Describe the morphology of the red blood cells.
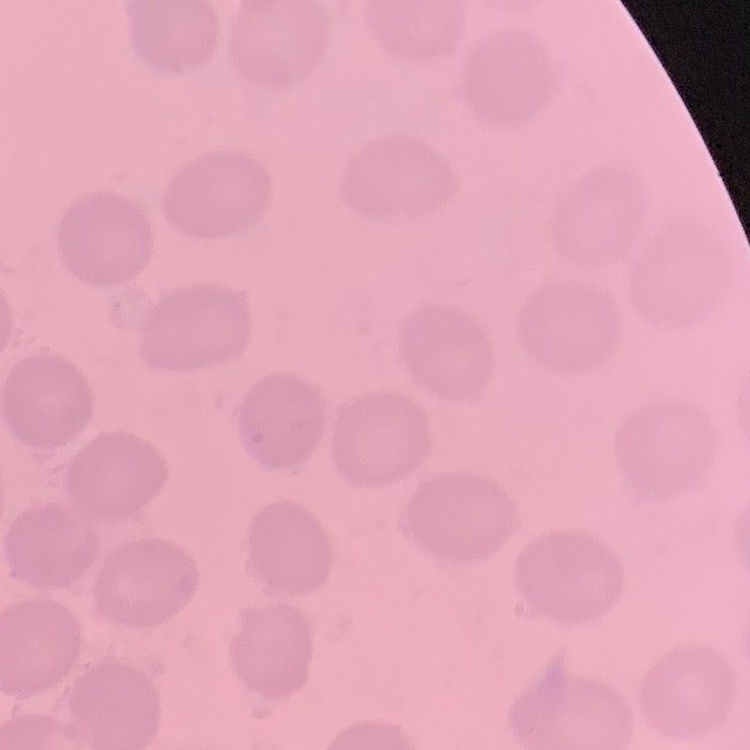

They show no rouleaux formation.

Stained with either Field's or Giemsa. One tile cut from a larger photomicrograph. Thin peripheral smear.